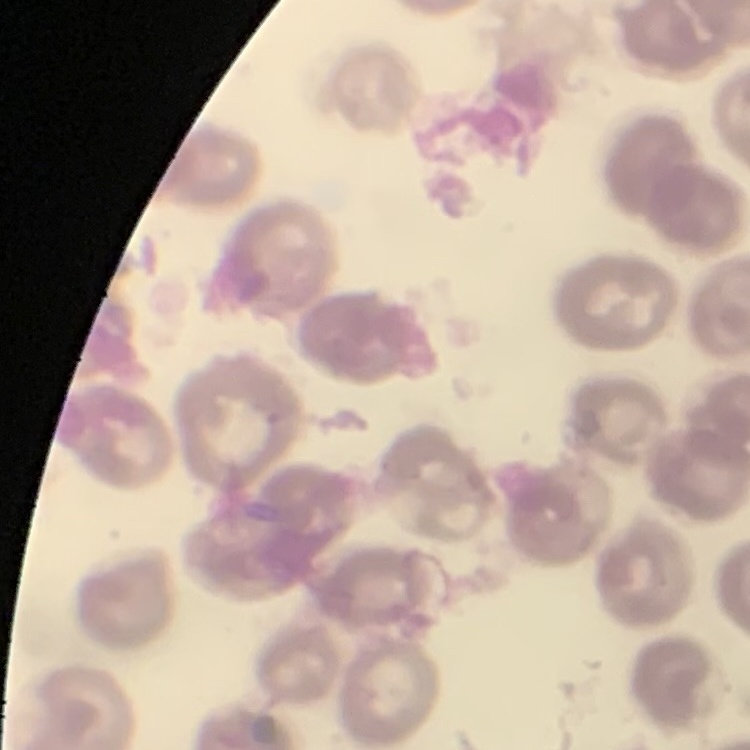

erythrocyte morphology = no rouleaux formation
preparation = thin blood film
stain = Field's or Giemsa
image type = square crop of a larger photomicrograph